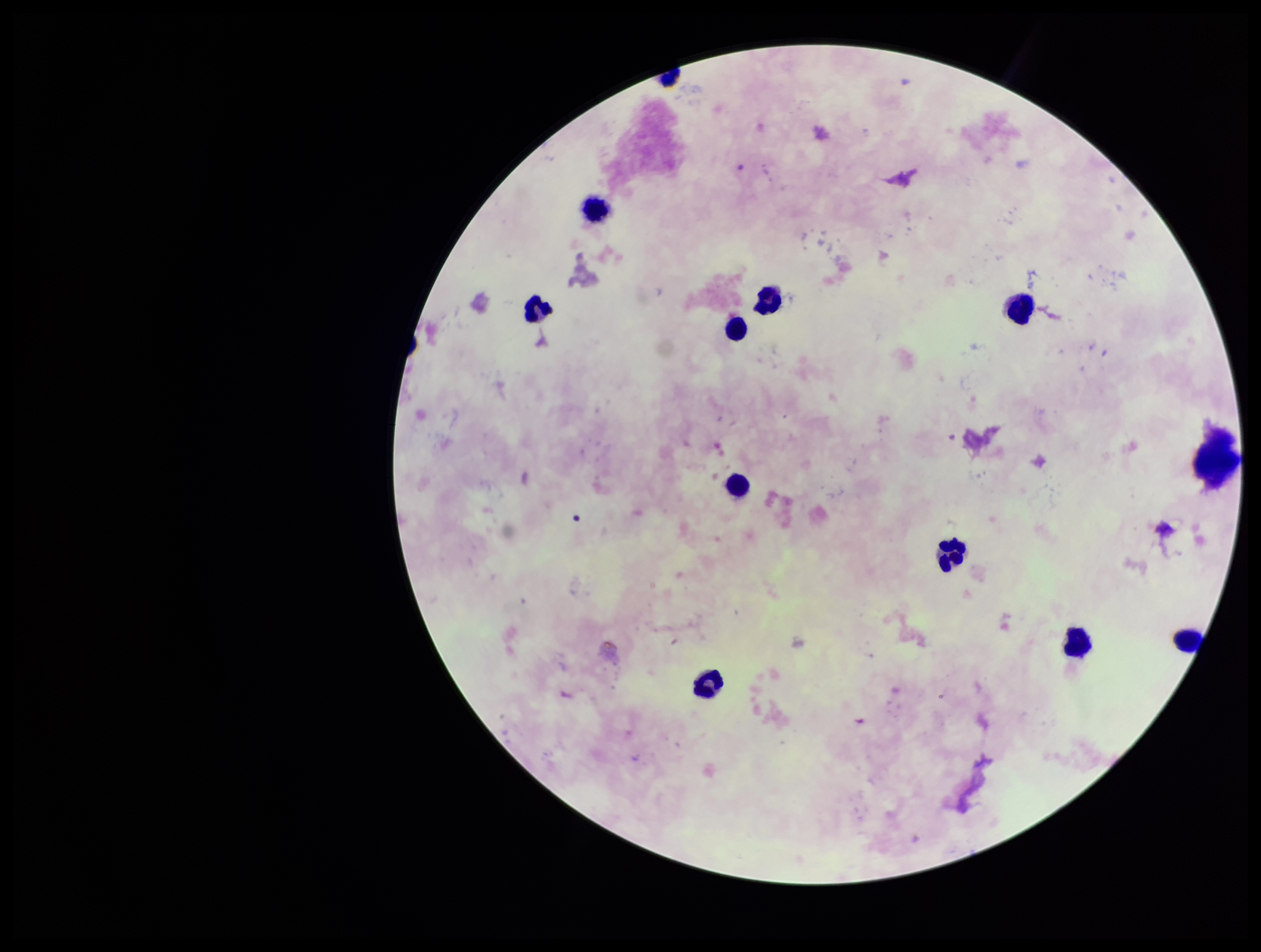

Plasmodium parasites = none identified
capture = smartphone photograph through the microscope eyepiece
preparation = thick smear
parasite count = 0
leukocyte count = 11
field of view = single
image size = 1261×952 pixels
stain = Giemsa
patient malaria status = negative